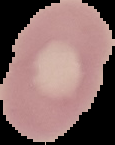

Summary:
  - Preparation: thin blood smear
  - Image size: 115×145 pixels
  - Result: negative for Plasmodium parasites
  - Image type: segmented cell region with the area outside set to black